Describe the morphology of the red blood cells.
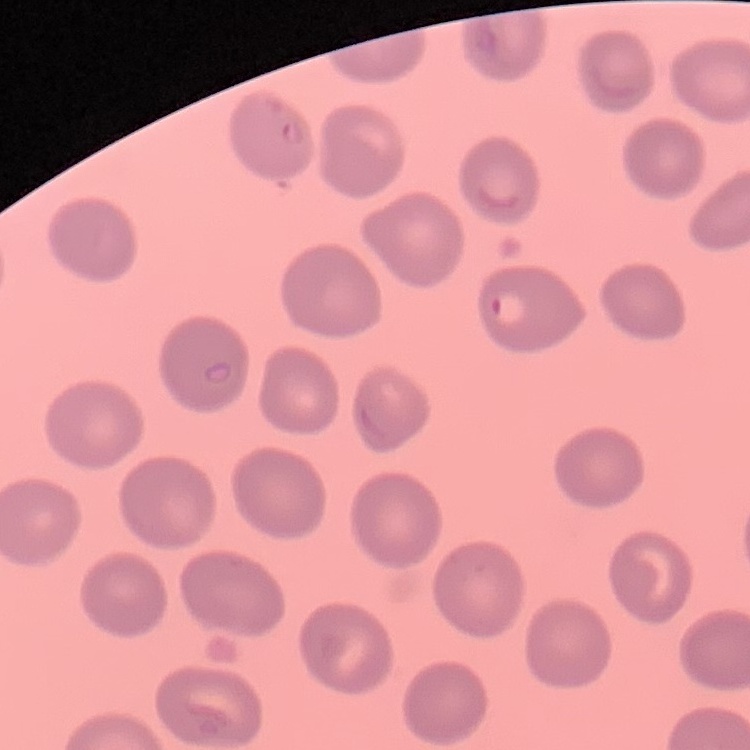
No rouleaux formation.

image type = one tile cut from a larger photomicrograph
preparation = thin peripheral smear
stain = Field's or Giemsa